Classify this cell by malaria status.
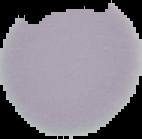

It is uninfected.

Cell region segmented out of the field of view; the surrounding area is masked to black. Image is 142×139 pixels. From a thin blood smear.